Report the malaria status of this cell.
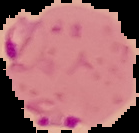
Parasitized.

image_type: cell region segmented out of the field of view; surrounding area masked to black
preparation: thin blood film
image_size: 139×133 pixels